Report the malaria status of this cell.
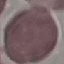
It is uninfected.

Thin blood smear. Automatically extracted cell patch, resized to 64 × 64 pixels. Giemsa stain. Acquired by smartphone through the microscope eyepiece.